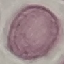
Summary:
  - Result: negative for malaria parasites
  - Preparation: thin blood film
  - Stain: Giemsa
  - Image type: cell patch, automatically extracted from a larger field of view and resized to 64 × 64 pixels
  - Capture: smartphone through the microscope eyepiece